Assess for malaria.
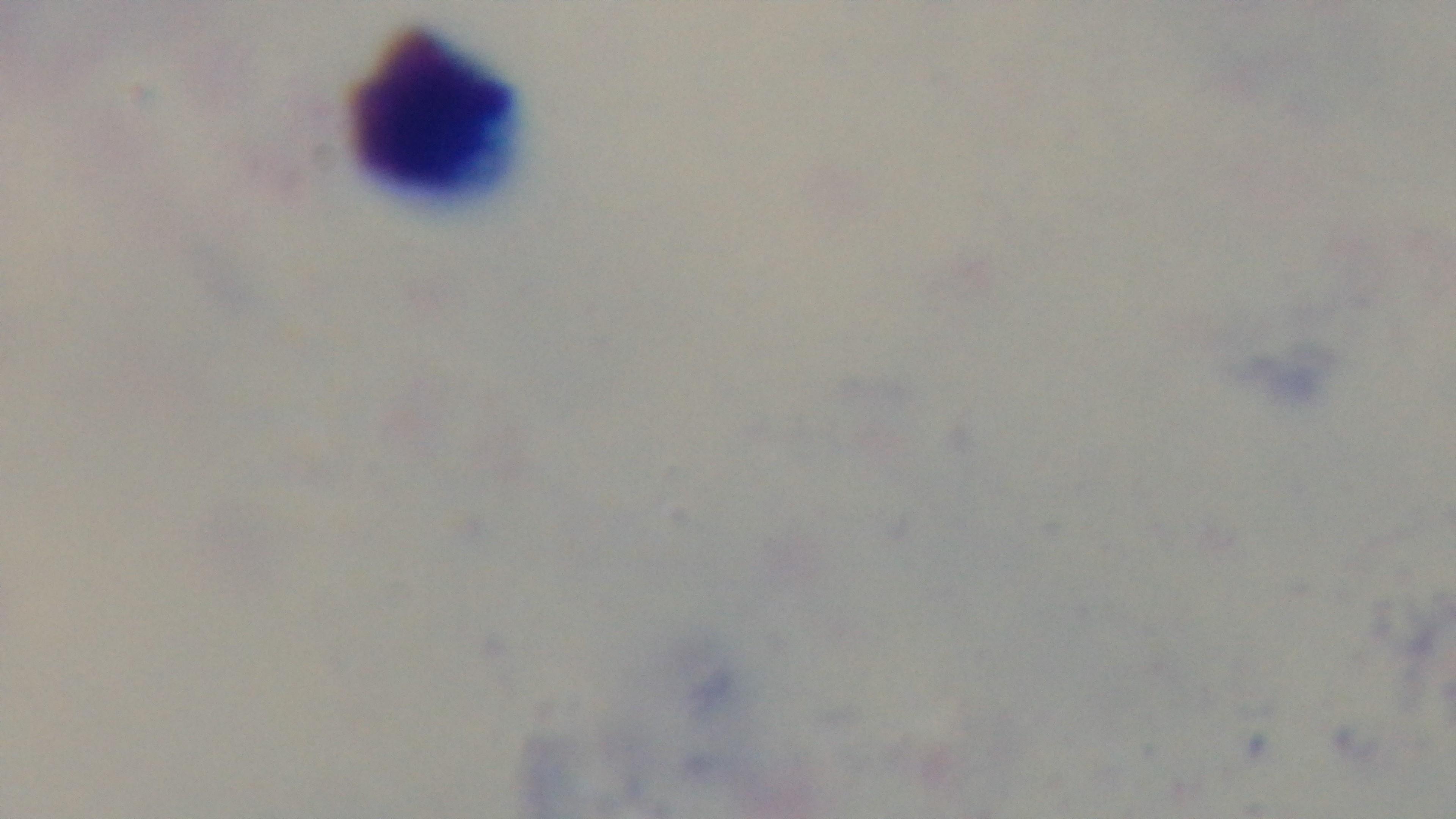

It is uninfected.

preparation = thick blood film
stain = Giemsa
capture = mounted 4K digital camera
field of view = one from the slide
modality = light microscopy
objective = 100x oil immersion